State which cell type is depicted.
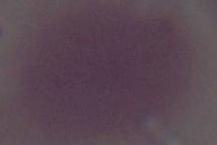
An erythrocyte.

magnification = 1000x
modality = photomicrograph